Locate and identify every blood parasite.
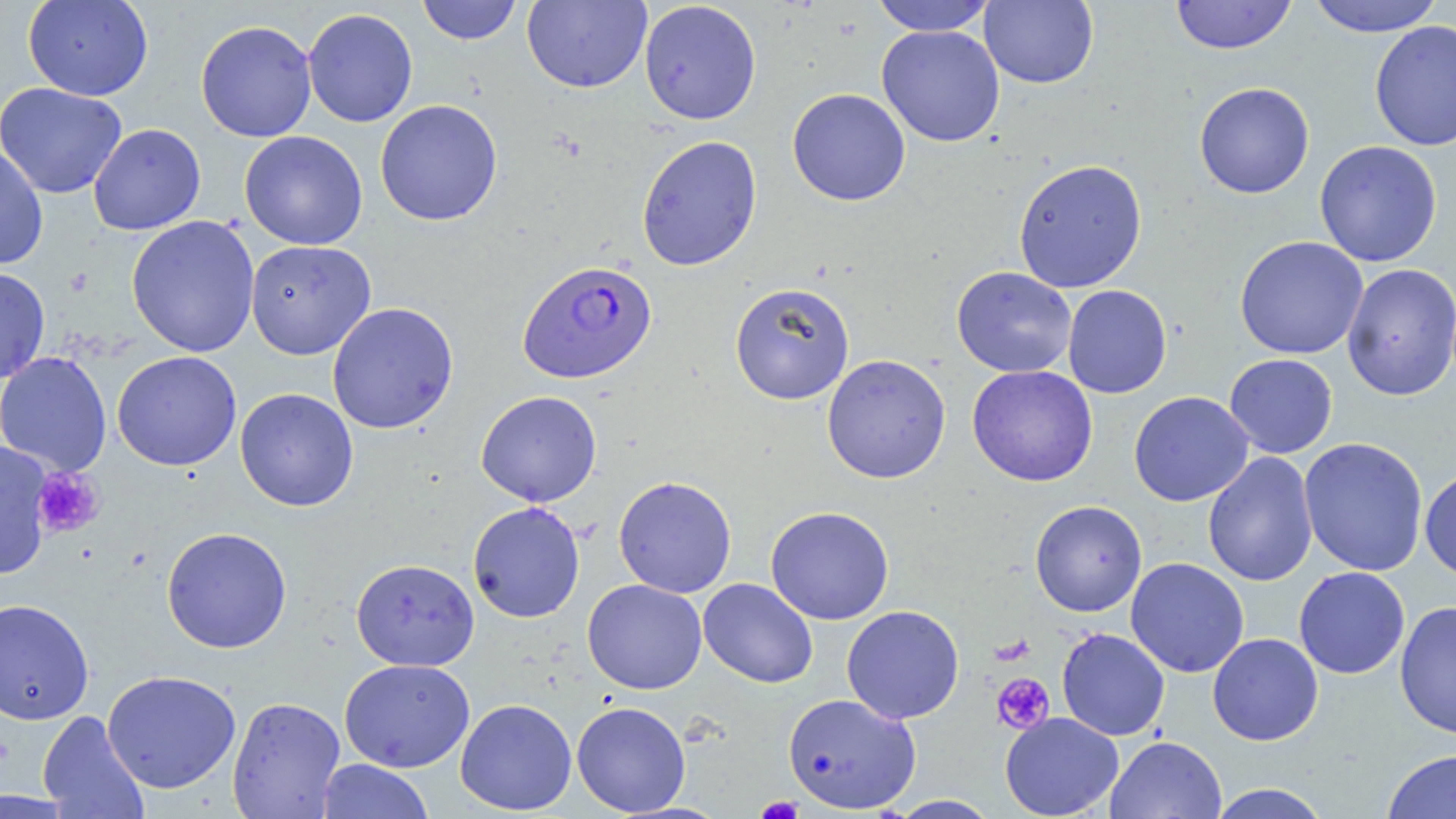
Approximate bounding boxes as (x1,y1)-(x2,y2) corner pairs in pixels.
Plasmodium falciparum-infected red blood cells: (517,259)-(657,383).
No Plasmodium ovale, Plasmodium malariae, Plasmodium vivax, Babesia divergens, or Trypanosoma brucei observed.

{
  "slide_level_diagnosis": "Plasmodium falciparum",
  "modality": "light microscopy",
  "magnification": "1000x",
  "preparation": "thin blood smear",
  "platelet_locations": "approximate bounding boxes as (x1,y1)-(x2,y2) corner pairs in pixels: (31,467)-(105,538), (992,673)-(1055,734), (755,797)-(805,818)",
  "field_of_view": "one of a larger specimen",
  "image_size": "1456×819 pixels",
  "uninfected_red_blood_cell_locations": "approximate bounding boxes as (x1,y1)-(x2,y2) corner pairs in pixels: (23,0)-(153,101), (417,0)-(523,45), (1170,0)-(1297,55), (1306,0)-(1444,37), (522,1)-(652,93), (638,1)-(762,125), (870,1)-(996,36), (979,1)-(1099,89), (302,8)-(418,127), (195,20)-(317,142), (1369,20)-(1456,152), (876,25)-(1005,147), (0,82)-(128,199), (1194,82)-(1314,199), (787,88)-(911,206), (375,99)-(503,226), (88,123)-(206,235), (239,130)-(368,250), (636,134)-(763,271), (1314,140)-(1443,267), (0,143)-(49,270), (1013,158)-(1148,293), (126,215)-(261,357), (1234,236)-(1368,359), (245,240)-(376,360), (1341,263)-(1456,401), (0,266)-(50,383), (951,266)-(1077,378), (730,282)-(855,404), (1062,285)-(1172,398), (326,301)-(459,434), (112,351)-(241,471), (0,352)-(113,476), (1224,353)-(1338,458), (822,354)-(951,484), (967,365)-(1098,487), (235,387)-(358,511), (476,390)-(602,507), (1129,391)-(1253,506), (1298,436)-(1428,576), (1,443)-(54,578), (1202,452)-(1319,587), (1419,468)-(1456,580), (613,475)-(737,598), (1030,500)-(1147,617), (467,501)-(585,623), (765,506)-(895,625), (161,526)-(292,653), (1125,557)-(1249,678), (351,558)-(480,672), (1293,566)-(1410,679), (698,577)-(818,688), (582,579)-(707,695), (0,598)-(94,725), (1395,600)-(1456,739), (841,605)-(965,724), (1057,628)-(1170,741), (1208,633)-(1323,746), (339,658)-(475,772), (102,670)-(241,793), (783,692)-(921,813), (226,696)-(346,818), (455,698)-(577,815), (571,701)-(691,816), (37,710)-(149,818), (999,712)-(1123,818), (1105,735)-(1227,819), (1382,749)-(1456,819), (316,759)-(435,819), (1206,783)-(1332,819), (886,795)-(1002,818)",
  "stain": "May-Grünwald-Giemsa"
}